Identify the preparation type.
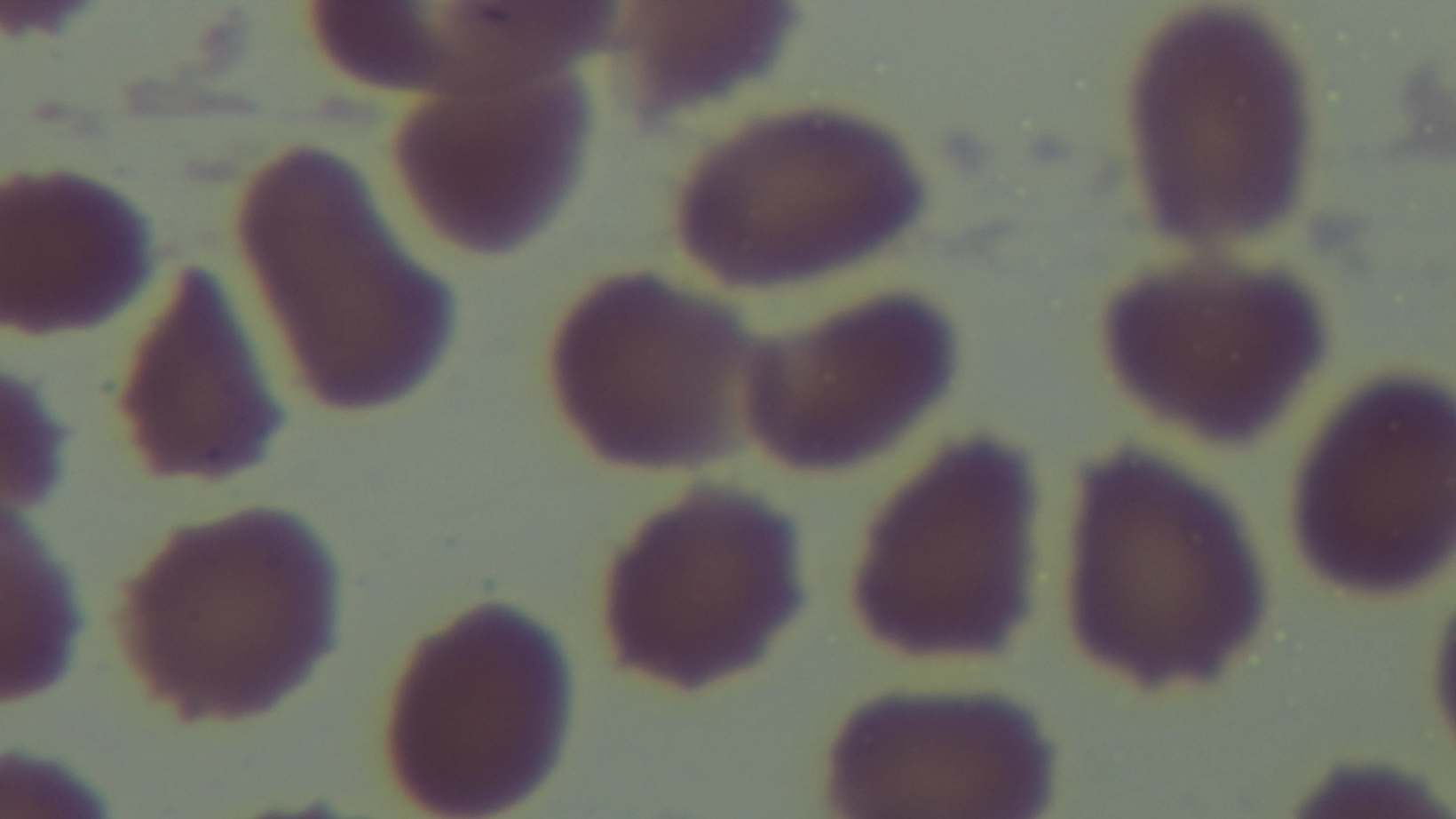

Thin.

Malaria status: negative. Giemsa stain. One field from the slide. Light microscopy. Mounted 4K digital camera. Oil-immersion objective, 100x.